Identify the blood parasite species.
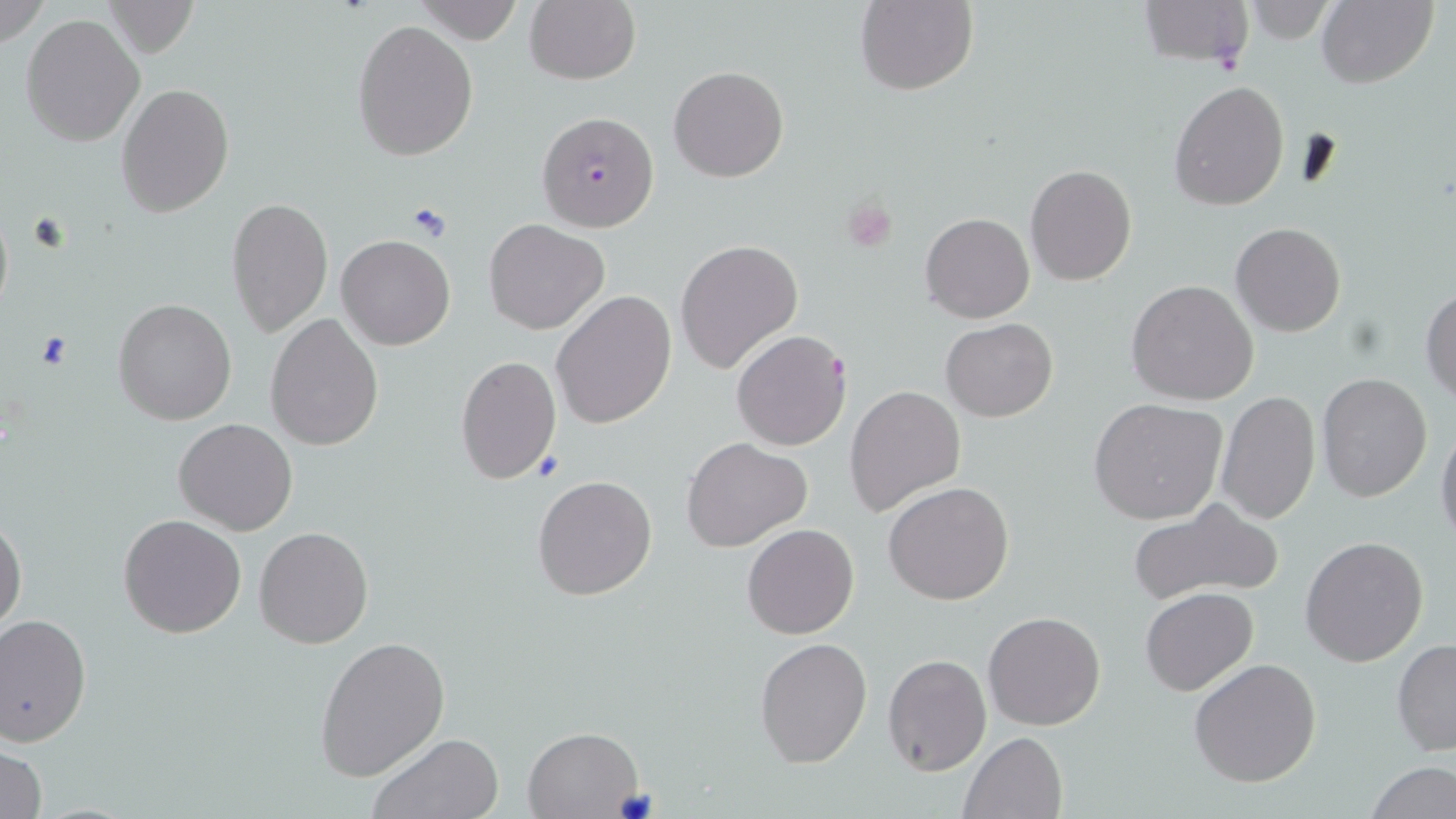
Plasmodium falciparum.

Summary:
  - Coordinate format: approximate bounding boxes as named x1/y1/x2/y2 corners in pixels
  - Uninfected red blood cell locations: (x1=0, y1=0, x2=49, y2=51), (x1=411, y1=0, x2=524, y2=43), (x1=525, y1=0, x2=640, y2=86), (x1=853, y1=0, x2=977, y2=96), (x1=1317, y1=0, x2=1437, y2=88), (x1=102, y1=1, x2=200, y2=58), (x1=1234, y1=3, x2=1343, y2=42), (x1=21, y1=14, x2=146, y2=147), (x1=352, y1=20, x2=477, y2=160), (x1=668, y1=65, x2=790, y2=182), (x1=1170, y1=80, x2=1289, y2=210), (x1=116, y1=82, x2=234, y2=218), (x1=1025, y1=164, x2=1136, y2=285), (x1=226, y1=198, x2=333, y2=337), (x1=921, y1=213, x2=1034, y2=324), (x1=484, y1=219, x2=609, y2=335), (x1=1230, y1=223, x2=1347, y2=336), (x1=337, y1=234, x2=454, y2=350), (x1=674, y1=238, x2=803, y2=373), (x1=1127, y1=280, x2=1259, y2=405), (x1=1420, y1=287, x2=1455, y2=403), (x1=550, y1=290, x2=677, y2=430), (x1=112, y1=298, x2=237, y2=424), (x1=264, y1=313, x2=382, y2=451), (x1=940, y1=319, x2=1058, y2=421), (x1=456, y1=354, x2=559, y2=485), (x1=1316, y1=373, x2=1432, y2=501), (x1=844, y1=384, x2=967, y2=518), (x1=1216, y1=392, x2=1320, y2=522), (x1=1088, y1=398, x2=1228, y2=525), (x1=173, y1=419, x2=298, y2=536), (x1=1436, y1=420, x2=1456, y2=547), (x1=683, y1=437, x2=811, y2=553), (x1=532, y1=474, x2=657, y2=601), (x1=884, y1=481, x2=1014, y2=605), (x1=1129, y1=501, x2=1286, y2=608), (x1=0, y1=513, x2=27, y2=636), (x1=118, y1=513, x2=247, y2=639), (x1=742, y1=523, x2=859, y2=640), (x1=253, y1=526, x2=374, y2=649), (x1=1300, y1=536, x2=1429, y2=668), (x1=1139, y1=587, x2=1259, y2=697), (x1=983, y1=610, x2=1107, y2=731), (x1=0, y1=611, x2=91, y2=747), (x1=314, y1=635, x2=450, y2=781), (x1=754, y1=637, x2=872, y2=768), (x1=1391, y1=638, x2=1456, y2=756), (x1=882, y1=654, x2=991, y2=775), (x1=1190, y1=658, x2=1322, y2=788), (x1=523, y1=727, x2=642, y2=818), (x1=959, y1=730, x2=1068, y2=819), (x1=364, y1=732, x2=504, y2=819), (x1=1, y1=741, x2=48, y2=819), (x1=1362, y1=761, x2=1454, y2=818)
  - Plasmodium falciparum-infected red blood cell locations: (x1=1139, y1=0, x2=1254, y2=73), (x1=537, y1=110, x2=659, y2=232), (x1=731, y1=329, x2=853, y2=450)
  - Platelet locations: (x1=842, y1=197, x2=898, y2=253), (x1=405, y1=201, x2=453, y2=242), (x1=33, y1=331, x2=75, y2=372)
  - Preparation: thin blood smear
  - Magnification: 1000x
  - Stain: May-Grünwald-Giemsa
  - Field of view: single
  - Modality: light microscopy
  - Image size: 1456×819 pixels